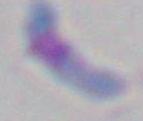 Toxoplasma gondii is seen. Photomicrograph. 1000x magnification.